Classify this cell by malaria status.
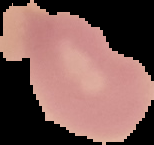
Uninfected.

Summary:
  - Preparation: thin blood smear
  - Image type: cell region segmented out of the field of view; surrounding area masked to black
  - Image size: 154×145 pixels